State which cell type is depicted.
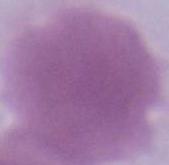
This is an erythrocyte.

Summary:
  - Modality: micrograph
  - Magnification: 1000x